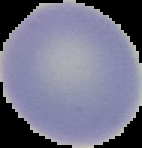

result = no Plasmodium parasites detected
image type = segmented cell region with the area outside set to black
preparation = thin blood film
image size = 142×148 pixels